Name the parasite shown.
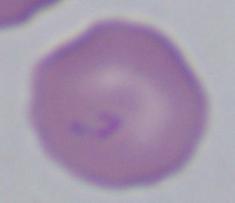

This is Babesia.

1000x magnification. Micrograph.